Classify this cell by malaria status.
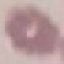

Uninfected.

capture = smartphone through the microscope eyepiece
image type = automatically extracted cell patch, resized to 64 × 64 pixels
preparation = thin blood smear
stain = Giemsa